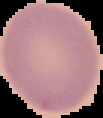

image size = 103×118 pixels
malaria status = uninfected
preparation = thin blood smear
image type = cell region segmented out of the field of view; surrounding area masked to black